Outline each uninfected red blood cell.
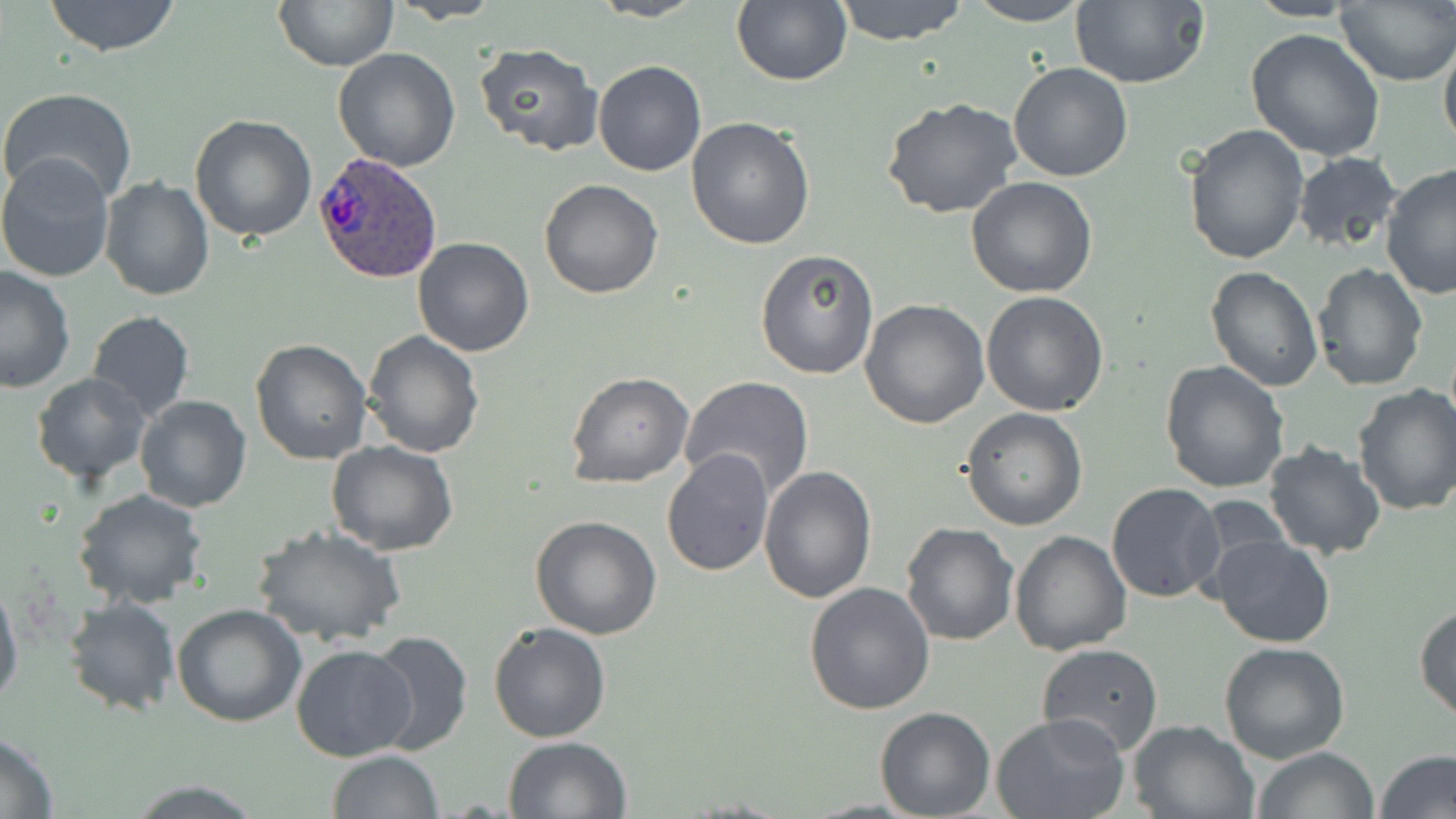
Approximate bounding boxes as [x1, y1, x2, y2] in pixels.
Uninfected red blood cells: [43, 0, 183, 56], [589, 0, 708, 22], [732, 0, 852, 85], [832, 0, 969, 45], [1069, 0, 1209, 89], [273, 1, 399, 70], [390, 1, 504, 23], [963, 1, 1093, 26], [1336, 2, 1456, 86], [1244, 27, 1388, 161], [1439, 31, 1456, 158], [473, 43, 604, 156], [332, 49, 461, 171], [592, 61, 707, 177], [1007, 62, 1134, 183], [1, 86, 138, 207], [881, 97, 1026, 221], [188, 114, 318, 243], [687, 116, 816, 250], [1184, 125, 1310, 266], [0, 151, 118, 284], [1291, 151, 1404, 257], [1379, 163, 1455, 300], [100, 175, 214, 302], [965, 175, 1098, 298], [539, 179, 664, 298], [411, 237, 536, 357], [755, 247, 879, 380], [1311, 261, 1429, 392], [0, 265, 77, 394], [1205, 266, 1322, 392], [981, 291, 1109, 415], [859, 298, 989, 430], [86, 311, 195, 424], [362, 332, 485, 459], [250, 338, 374, 465], [1158, 360, 1289, 494], [567, 372, 694, 488], [31, 373, 152, 487], [679, 376, 816, 500], [1352, 383, 1456, 518], [135, 394, 251, 512], [960, 408, 1087, 530], [324, 439, 458, 556], [1262, 439, 1388, 561], [662, 448, 774, 576], [759, 466, 877, 604], [1106, 483, 1226, 603], [70, 489, 209, 609], [531, 516, 663, 639], [900, 521, 1019, 646], [252, 523, 406, 647], [1008, 530, 1132, 655], [1209, 533, 1335, 648], [0, 574, 23, 714], [804, 583, 935, 716], [63, 596, 180, 716], [171, 603, 306, 727], [1414, 603, 1456, 724], [488, 621, 611, 743], [364, 631, 473, 756], [1037, 642, 1165, 756], [1218, 643, 1350, 764], [290, 644, 417, 763], [874, 707, 996, 819], [992, 713, 1131, 819], [1127, 718, 1259, 818], [0, 732, 58, 816], [502, 736, 632, 818], [1250, 746, 1380, 819], [325, 749, 443, 818], [1376, 750, 1456, 819], [125, 780, 265, 816].

slide-level diagnosis = Plasmodium ovale
image size = 1456×819 pixels
Plasmodium ovale-infected red blood cell locations = approximate bounding boxes as [x1, y1, x2, y2] in pixels: [314, 150, 442, 284]
magnification = 1000x
preparation = thin blood smear
field of view = one of a larger specimen
stain = May-Grünwald-Giemsa
modality = light microscopy